Locate and identify every blood parasite.
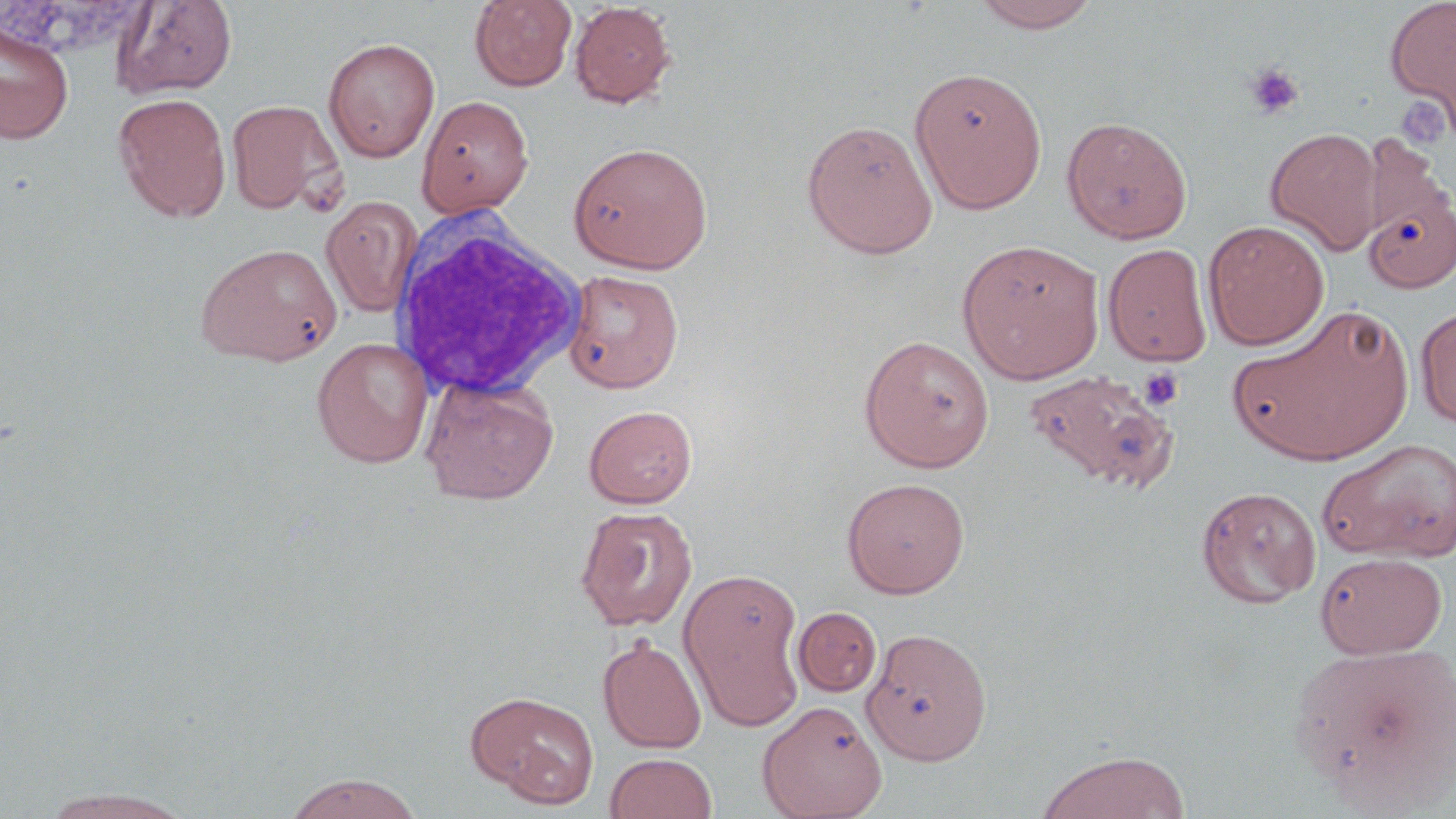
No blood parasites observed.

Approximate bounding boxes as (x1,y1)-(x2,y2) corner pairs in pixels. Uninfected red blood cell locations: (469,0)-(577,91), (970,0)-(1102,33), (1385,0)-(1456,133), (112,1)-(238,98), (569,2)-(677,108), (0,20)-(75,145), (323,38)-(440,162), (909,66)-(1048,214), (113,93)-(231,221), (416,95)-(534,217), (226,100)-(343,215), (1061,115)-(1193,244), (801,118)-(938,258), (1264,127)-(1384,255), (568,141)-(713,273), (1363,191)-(1456,293), (321,196)-(423,317), (1203,220)-(1329,350), (956,239)-(1105,384), (197,243)-(341,366), (1103,243)-(1212,366), (562,269)-(683,392), (1229,303)-(1416,467), (1416,305)-(1456,429), (858,335)-(995,472), (312,336)-(434,468), (1023,368)-(1179,491), (420,375)-(559,505), (584,405)-(697,508), (1319,438)-(1456,563), (841,477)-(970,598), (1196,485)-(1321,608), (575,506)-(697,631), (1315,551)-(1448,658), (680,568)-(805,725), (793,607)-(882,697), (861,627)-(992,766), (598,636)-(707,753), (1288,640)-(1455,804), (466,690)-(600,807), (757,700)-(887,818), (1035,751)-(1190,819), (604,753)-(718,818), (284,772)-(423,818), (39,788)-(195,818). Platelet locations: (1244,62)-(1305,120), (1395,97)-(1451,152), (1138,366)-(1184,411). White blood cell locations: (385,212)-(590,400). Slide-level diagnosis: no evidence of blood parasites. Optical microscopy. Captured at 1000x magnification. May-Grünwald-Giemsa-stained preparation. Thin blood smear. Single field of view. Image is 1456×819 pixels.